Assess the morphology of the red blood cells.
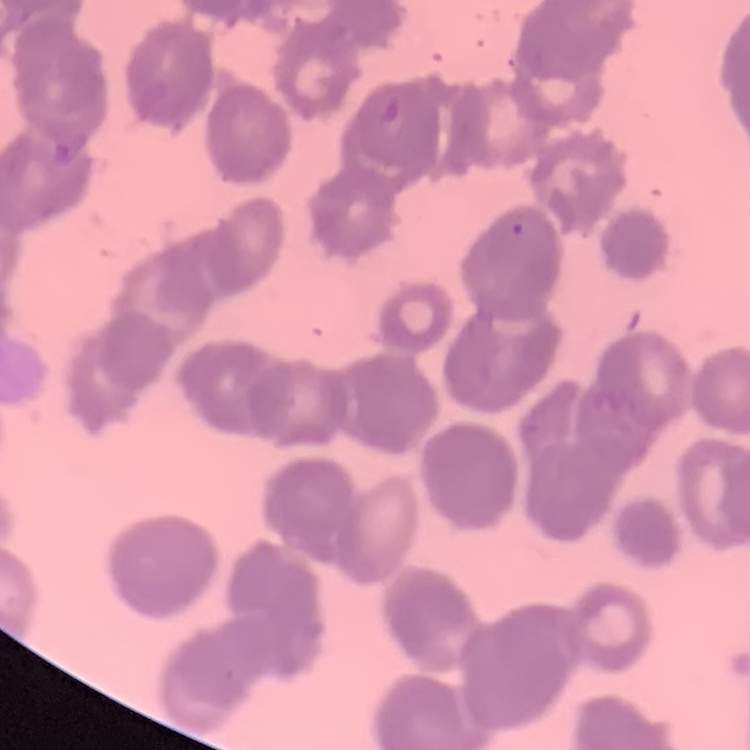
Rouleaux formation.

Summary:
  - Preparation: thin blood film
  - Image type: one tile cut from a larger photomicrograph
  - Stain: Field's or Giemsa